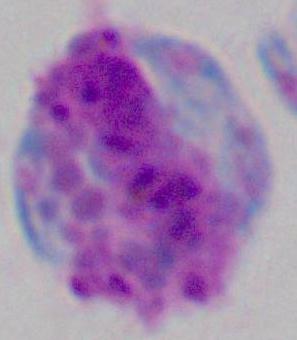

Summary:
  - Magnification: 1000x
  - Modality: micrograph
  - Identification: white blood cell